State which parasite is depicted.
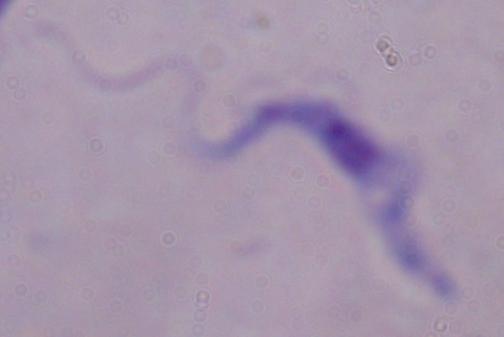
This is a trypanosome.

modality = photomicrograph
magnification = 1000x